Identify the cell.
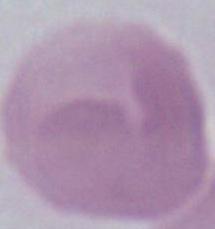

An erythrocyte.

Summary:
  - Magnification: 1000x
  - Modality: photomicrograph